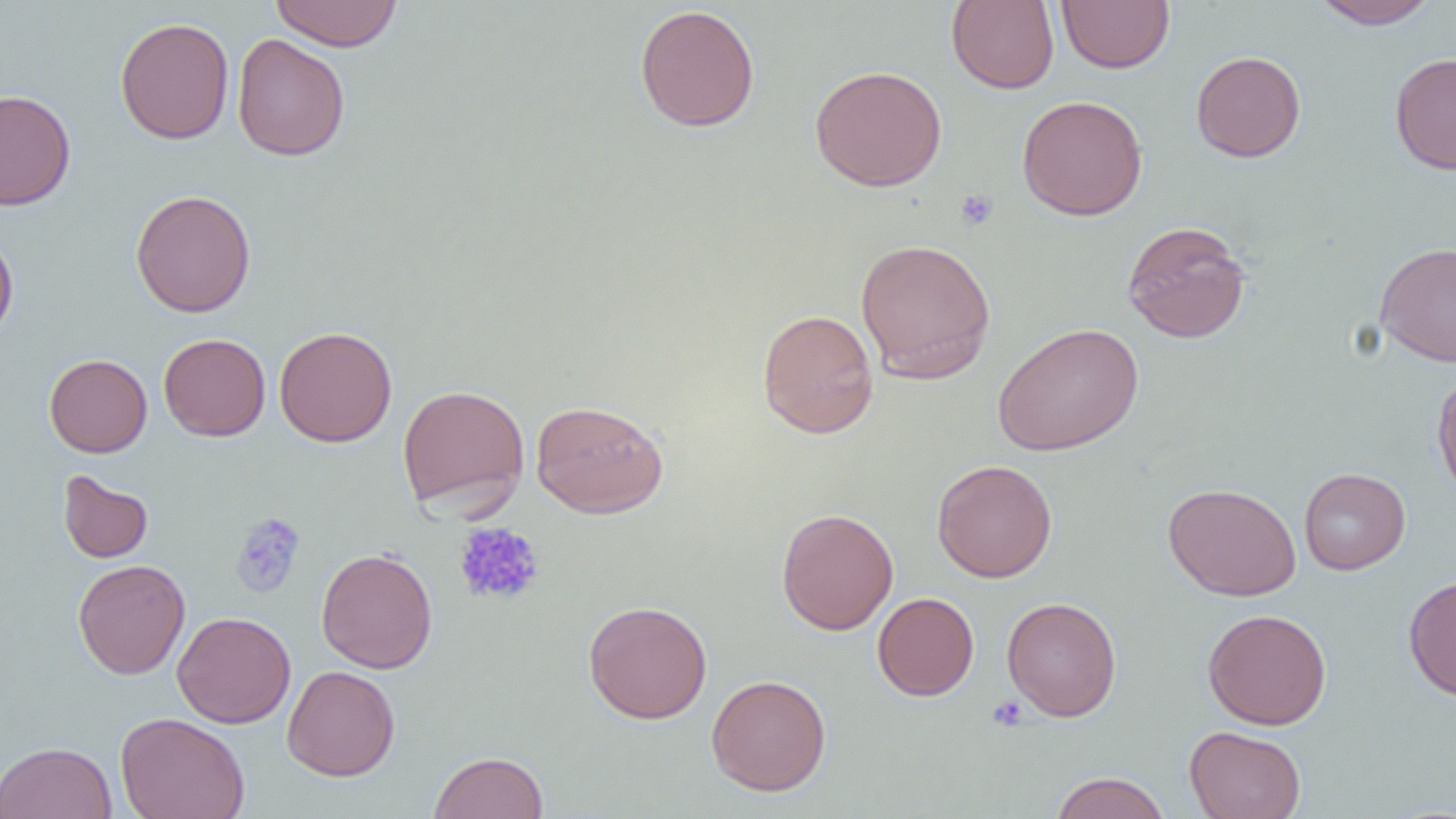

slide-level diagnosis = negative for blood parasites
platelet locations = approximate bounding boxes as named x1/y1/x2/y2 corners in pixels: (x1=955, y1=189, x2=999, y2=231), (x1=229, y1=512, x2=306, y2=599), (x1=453, y1=521, x2=545, y2=607), (x1=987, y1=695, x2=1029, y2=732)
preparation = thin blood smear
magnification = 1000x
uninfected red blood cell locations = approximate bounding boxes as named x1/y1/x2/y2 corners in pixels: (x1=269, y1=0, x2=402, y2=52), (x1=1056, y1=0, x2=1175, y2=74), (x1=1310, y1=0, x2=1440, y2=30), (x1=946, y1=1, x2=1059, y2=93), (x1=634, y1=4, x2=760, y2=132), (x1=114, y1=16, x2=234, y2=145), (x1=231, y1=33, x2=350, y2=161), (x1=1190, y1=50, x2=1306, y2=163), (x1=1390, y1=51, x2=1456, y2=174), (x1=809, y1=65, x2=948, y2=191), (x1=0, y1=88, x2=76, y2=210), (x1=1017, y1=94, x2=1148, y2=220), (x1=130, y1=189, x2=256, y2=317), (x1=1121, y1=220, x2=1251, y2=344), (x1=0, y1=227, x2=19, y2=344), (x1=855, y1=238, x2=996, y2=384), (x1=1374, y1=241, x2=1455, y2=367), (x1=757, y1=309, x2=879, y2=438), (x1=991, y1=322, x2=1143, y2=456), (x1=274, y1=325, x2=398, y2=447), (x1=159, y1=333, x2=271, y2=441), (x1=44, y1=353, x2=153, y2=457), (x1=1432, y1=370, x2=1456, y2=503), (x1=397, y1=383, x2=530, y2=515), (x1=530, y1=399, x2=668, y2=518), (x1=932, y1=459, x2=1057, y2=582), (x1=1298, y1=467, x2=1411, y2=575), (x1=57, y1=469, x2=154, y2=564), (x1=1162, y1=483, x2=1301, y2=601), (x1=776, y1=508, x2=899, y2=635), (x1=316, y1=548, x2=438, y2=674), (x1=73, y1=559, x2=190, y2=679), (x1=1403, y1=574, x2=1456, y2=702), (x1=872, y1=592, x2=979, y2=701), (x1=1002, y1=596, x2=1121, y2=722), (x1=583, y1=600, x2=713, y2=724), (x1=1203, y1=608, x2=1332, y2=730), (x1=172, y1=611, x2=296, y2=729), (x1=282, y1=665, x2=400, y2=781), (x1=706, y1=674, x2=831, y2=796), (x1=115, y1=711, x2=250, y2=819), (x1=1184, y1=725, x2=1306, y2=819), (x1=0, y1=741, x2=117, y2=819), (x1=429, y1=751, x2=548, y2=819), (x1=1049, y1=771, x2=1171, y2=819)
field of view = one of a larger specimen
modality = optical microscopy
image size = 1456×819 pixels